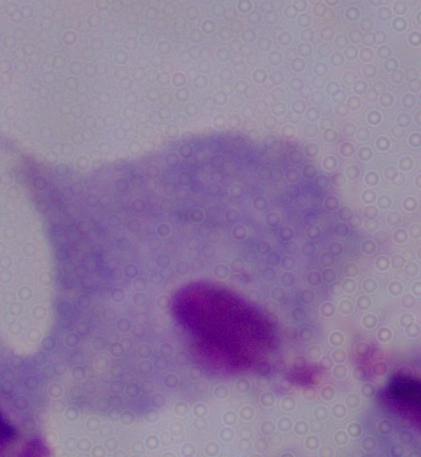

Summary:
  - Identification: trichomonad
  - Modality: micrograph
  - Magnification: 1000x